Describe the morphology of the red blood cells.
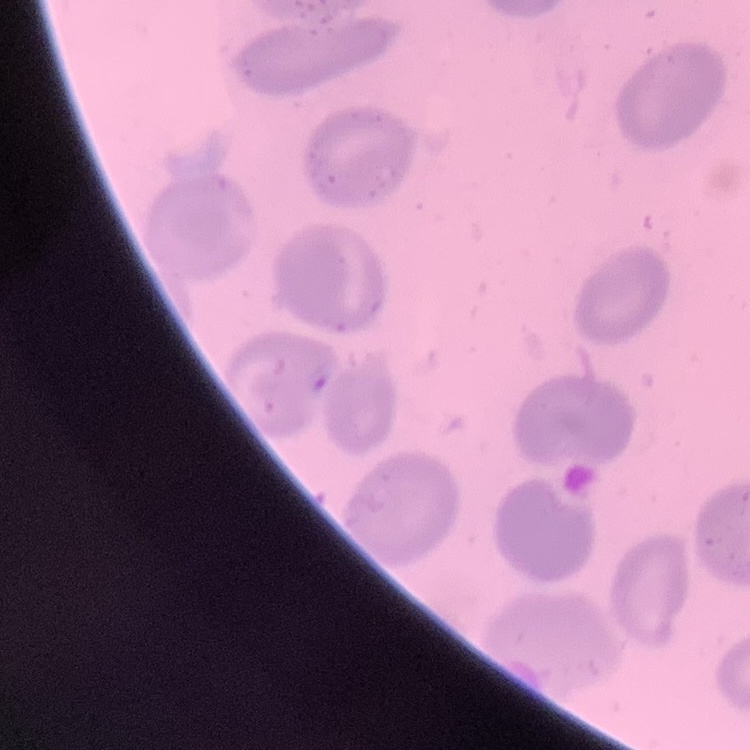

No rouleaux formation.

preparation = thin blood film
image type = one tile cut from a larger photomicrograph
stain = Field's or Giemsa